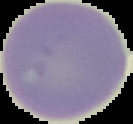

image type = segmented cell region on a black background
preparation = thin blood smear
image size = 133×124 pixels
malaria status = uninfected